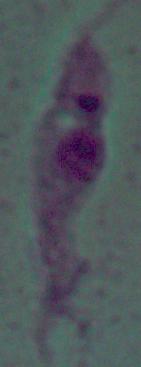
{
  "magnification": "1000x",
  "modality": "micrograph",
  "identification": "Leishmania"
}